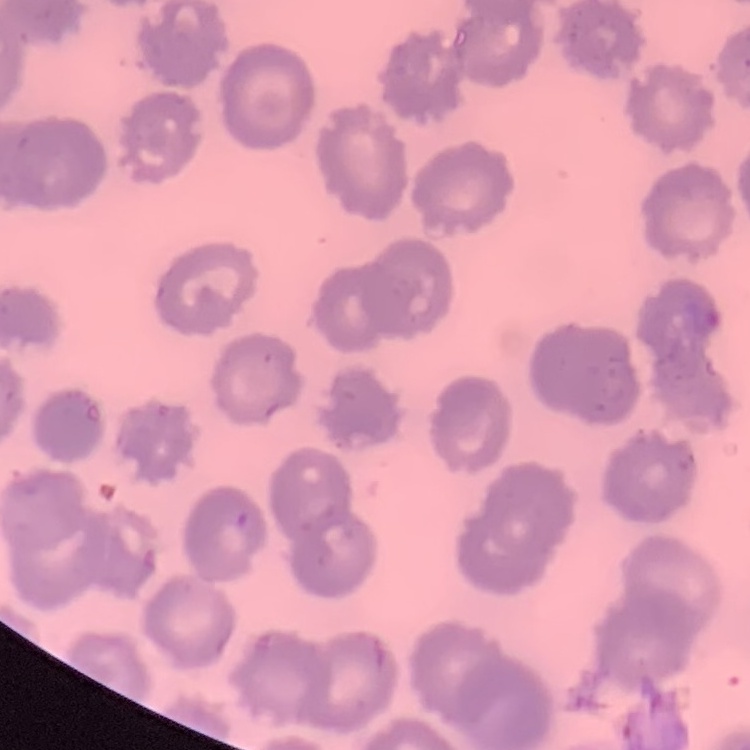 The erythrocytes exhibit no rouleaux formation. One tile cut from a larger photomicrograph. Stained with either Field's or Giemsa. Thin blood film.